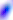

{
  "identification": "Toxoplasma gondii",
  "modality": "micrograph",
  "magnification": "400x"
}